Name the parasite shown.
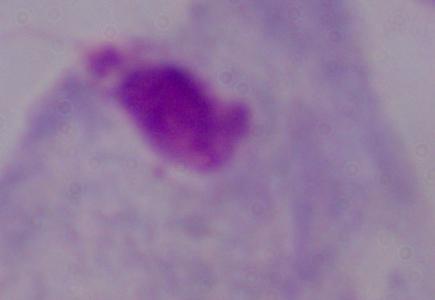
This is a trichomonad.

Micrograph. 1000x magnification.